Report the malaria status of this cell.
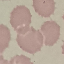
Uninfected.

Summary:
  - Capture: smartphone through the microscope eyepiece
  - Stain: Giemsa
  - Preparation: thin smear
  - Image type: cell patch, automatically extracted from a larger field of view and resized to 64 × 64 pixels